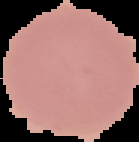

Summary:
  - Image type: cell region segmented out of the field of view; surrounding area masked to black
  - Preparation: thin blood film
  - Image size: 139×142 pixels
  - Result: negative for Plasmodium parasites